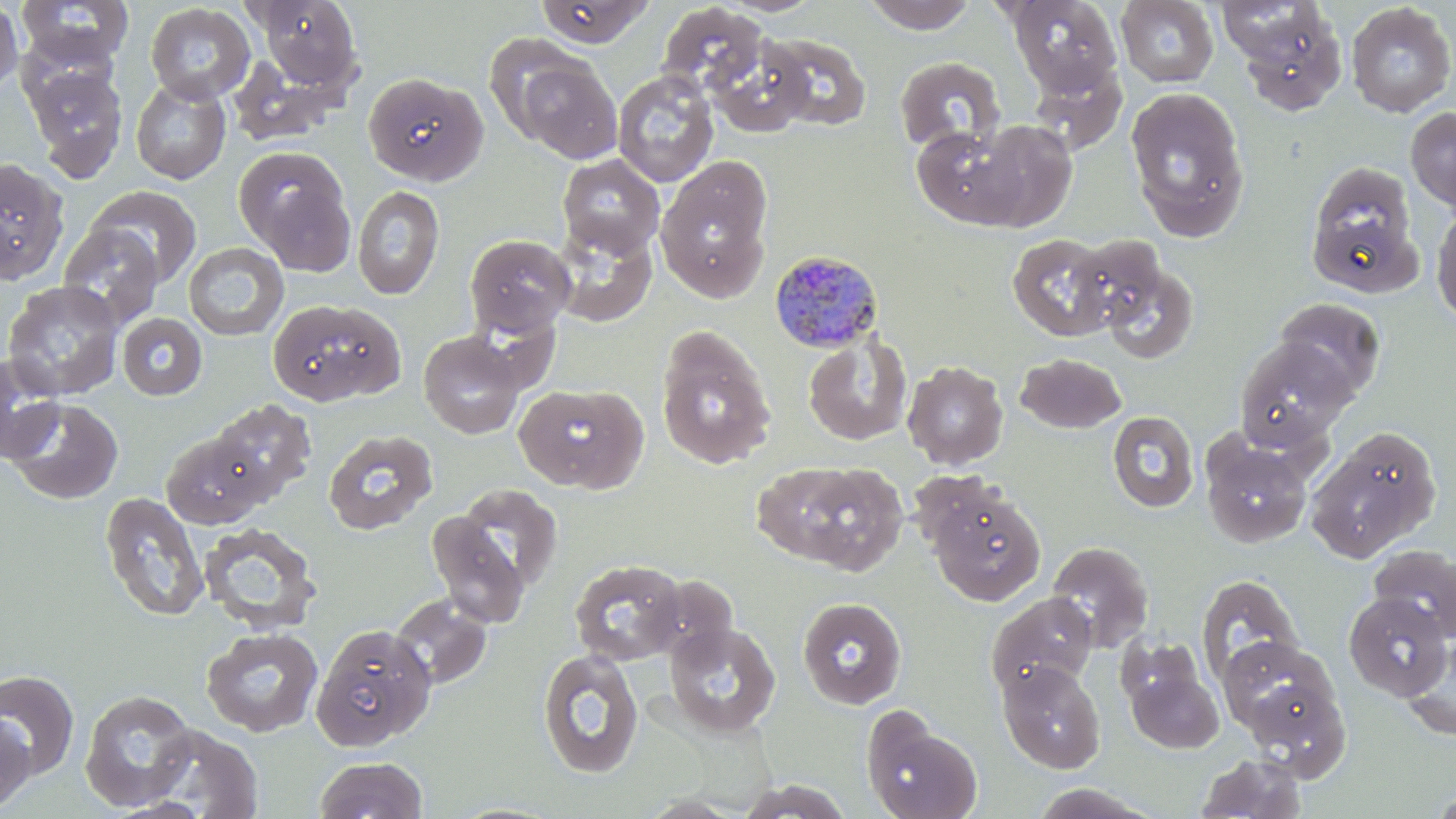
slide-level diagnosis = Plasmodium malariae
stain = May-Grünwald-Giemsa
field of view = one of a larger specimen
magnification = 1000x
modality = light microscopy
preparation = thin blood smear
Plasmodium malariae-infected red blood cell locations = approximate bounding boxes as (x1, y1, x2, y2) in pixels: (769, 248, 884, 353)
uninfected red blood cell locations = approximate bounding boxes as (x1, y1, x2, y2) in pixels: (0, 0, 24, 98), (16, 0, 134, 70), (250, 0, 364, 93), (861, 0, 979, 33), (1006, 0, 1122, 97), (1115, 0, 1219, 87), (534, 1, 654, 48), (1220, 1, 1350, 114), (145, 3, 256, 103), (657, 3, 769, 100), (1346, 3, 1456, 117), (763, 32, 872, 131), (706, 33, 812, 138), (484, 34, 594, 144), (227, 52, 353, 146), (514, 55, 623, 163), (894, 55, 1006, 154), (23, 60, 129, 182), (1027, 61, 1127, 153), (612, 70, 719, 188), (362, 72, 487, 185), (130, 77, 231, 185), (1125, 86, 1250, 240), (1406, 107, 1456, 212), (972, 119, 1077, 232), (911, 125, 1023, 229), (233, 146, 355, 267), (558, 154, 665, 259), (656, 156, 774, 303), (0, 157, 69, 284), (1305, 160, 1422, 295), (353, 185, 445, 300), (88, 187, 202, 288), (1430, 203, 1456, 327), (550, 219, 657, 328), (57, 222, 165, 326), (464, 233, 577, 338), (1006, 233, 1119, 341), (1067, 233, 1170, 334), (183, 242, 289, 341), (1095, 257, 1200, 364), (2, 280, 125, 401), (268, 298, 407, 406), (1274, 298, 1385, 399), (117, 313, 208, 400), (655, 329, 776, 469), (418, 331, 526, 438), (803, 333, 912, 446), (1234, 337, 1356, 450), (0, 353, 65, 464), (1015, 353, 1127, 433), (902, 360, 1008, 469), (515, 383, 648, 494), (4, 397, 124, 505), (207, 400, 317, 505), (1107, 410, 1199, 513), (322, 429, 438, 535), (1307, 430, 1440, 562), (161, 431, 270, 528), (1200, 434, 1313, 548), (751, 458, 908, 575), (453, 483, 564, 593), (925, 484, 1046, 606), (99, 492, 209, 622), (427, 514, 531, 628), (199, 522, 322, 634), (1045, 540, 1154, 652), (1369, 544, 1456, 641), (569, 558, 686, 666), (1196, 573, 1304, 687), (647, 574, 739, 664), (1343, 591, 1452, 701), (985, 592, 1098, 698), (389, 594, 493, 690), (797, 597, 907, 710), (664, 621, 782, 738), (312, 623, 437, 750), (200, 628, 324, 738), (1401, 636, 1456, 740), (1220, 637, 1340, 740), (536, 649, 644, 779), (1123, 655, 1224, 753), (997, 660, 1106, 774), (0, 671, 80, 781), (80, 690, 199, 811), (861, 709, 983, 819), (0, 716, 35, 811), (144, 725, 263, 819), (1195, 753, 1309, 818), (312, 756, 429, 818), (733, 778, 856, 818), (1026, 783, 1163, 818), (1430, 789, 1456, 818), (444, 801, 566, 819)
image size = 1456×819 pixels